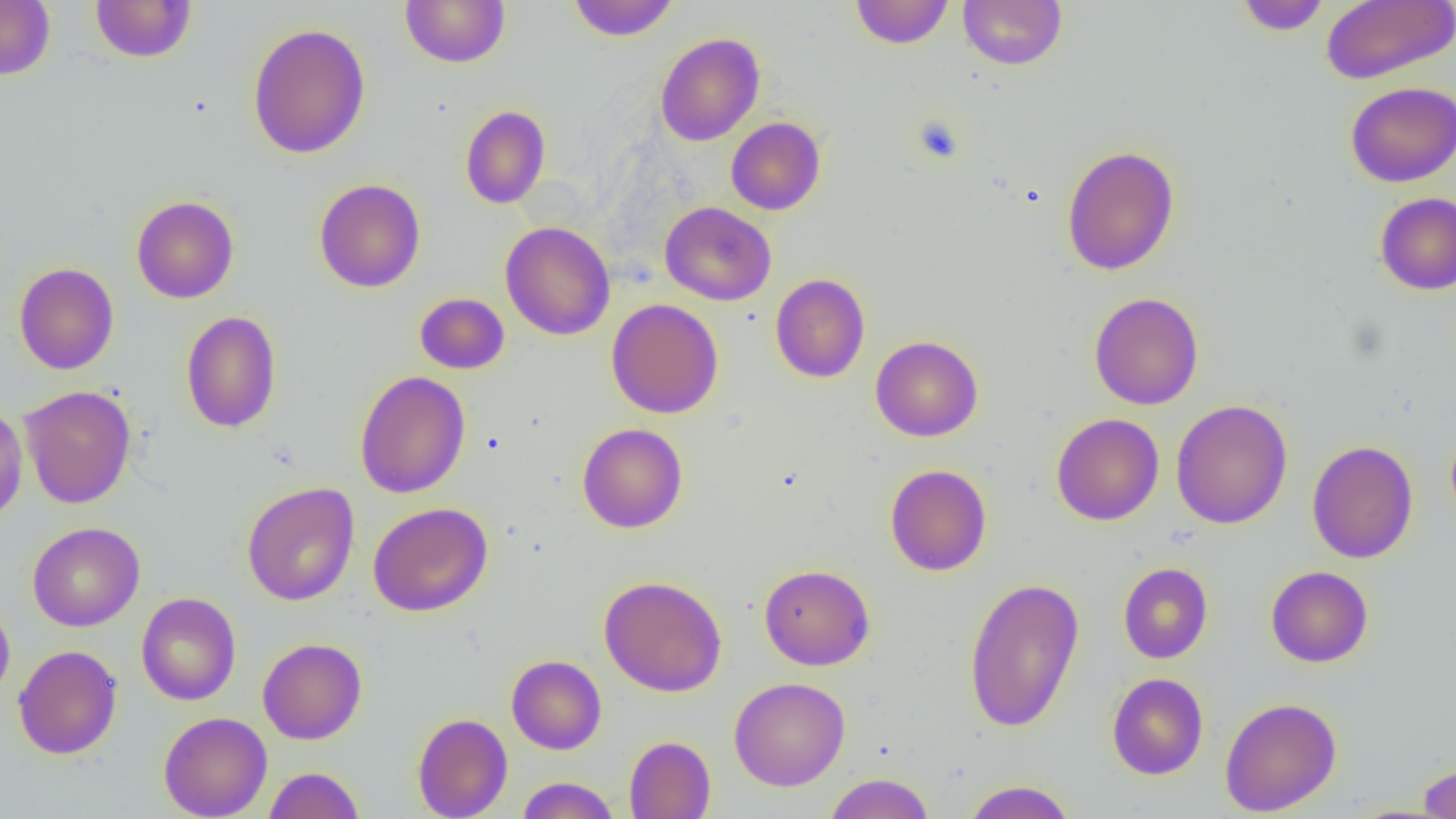
slide-level diagnosis = negative for blood parasites
uninfected red blood cell locations = approximate bounding boxes as (x1, y1, x2, y2) in pixels: (0, 0, 55, 80), (89, 0, 197, 63), (400, 0, 510, 68), (567, 0, 679, 42), (850, 0, 954, 49), (958, 0, 1067, 70), (1235, 0, 1332, 35), (1321, 1, 1455, 84), (247, 22, 371, 159), (654, 32, 765, 146), (1345, 81, 1456, 187), (460, 105, 551, 209), (726, 117, 826, 215), (1061, 145, 1180, 275), (314, 178, 426, 293), (1374, 192, 1456, 295), (131, 195, 239, 304), (660, 202, 776, 306), (500, 222, 615, 340), (14, 262, 119, 375), (770, 273, 870, 383), (414, 292, 510, 374), (1089, 292, 1204, 410), (606, 298, 724, 419), (181, 310, 282, 433), (870, 335, 983, 442), (354, 370, 471, 499), (19, 385, 137, 509), (1171, 399, 1293, 530), (0, 404, 28, 526), (1051, 413, 1164, 526), (577, 423, 688, 533), (1306, 440, 1419, 564), (885, 464, 992, 576), (242, 482, 360, 606), (368, 502, 493, 617), (27, 522, 145, 631), (1118, 562, 1213, 663), (759, 564, 875, 670), (1265, 566, 1374, 667), (598, 575, 727, 697), (963, 576, 1085, 732), (136, 592, 241, 705), (0, 600, 15, 706), (258, 637, 367, 745), (13, 645, 122, 759), (506, 654, 607, 754), (1106, 672, 1209, 780), (729, 677, 850, 791), (1219, 696, 1342, 816), (158, 711, 272, 818), (412, 712, 513, 819), (624, 735, 716, 818), (1417, 762, 1456, 818), (263, 766, 365, 819), (823, 773, 936, 819), (516, 777, 620, 818), (960, 780, 1078, 819)
preparation = thin blood smear
image size = 1456×819 pixels
modality = light microscopy
field of view = single
magnification = 1000x